Assess this cell for malaria.
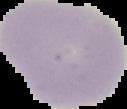

Uninfected.

image_type: segmented cell region with the area outside set to black
image_size: 127×109 pixels
preparation: thin blood smear